Identify the parasite.
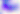

This is Toxoplasma gondii.

Summary:
  - Magnification: 400x
  - Modality: micrograph